Locate every blood parasite and identify its species.
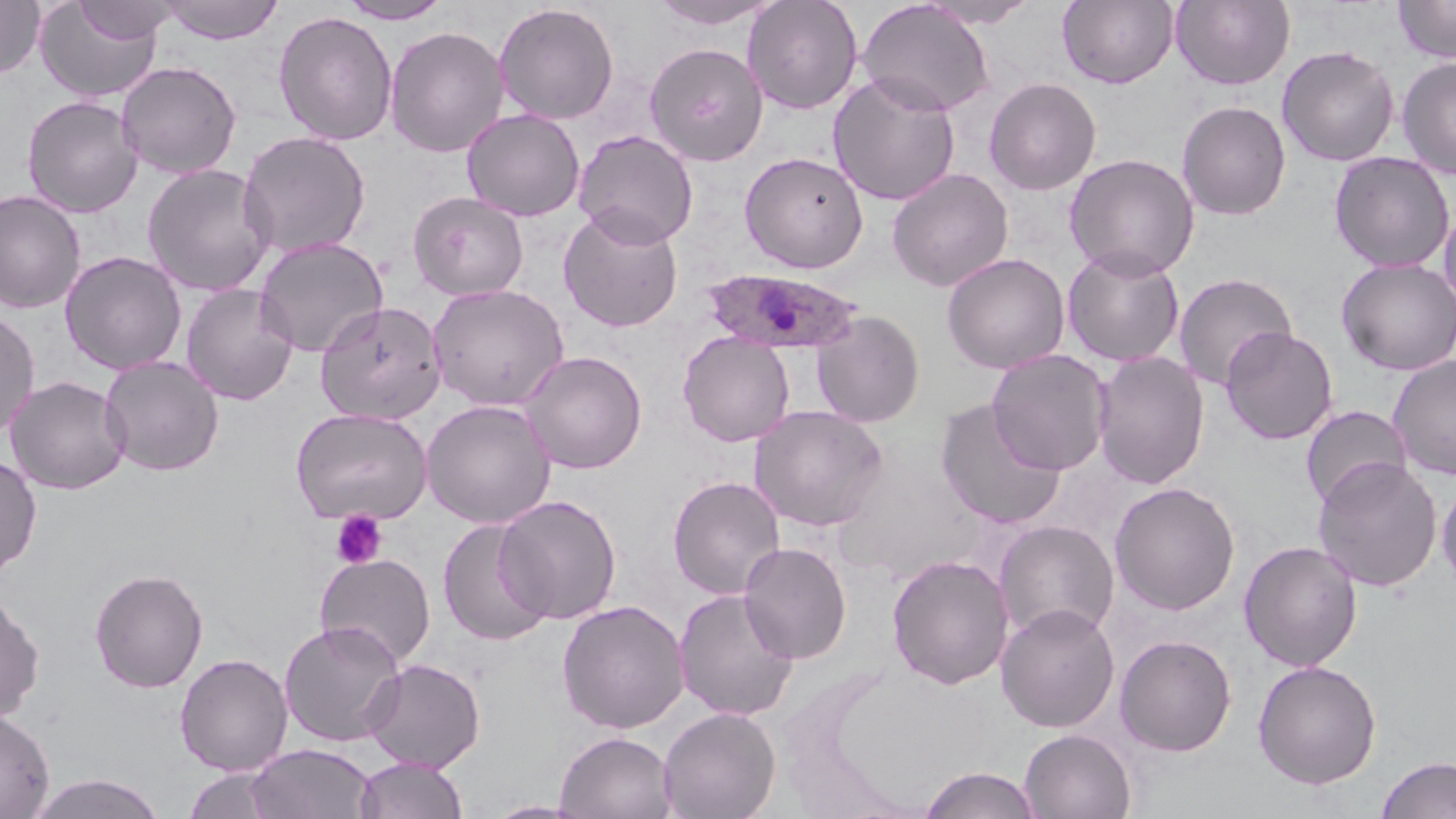

Approximate bounding boxes as [x1, y1, x2, y2] in pixels.
Plasmodium ovale-infected red blood cells: [703, 268, 865, 355].
No Plasmodium falciparum, Plasmodium malariae, Plasmodium vivax, Babesia divergens, or Trypanosoma brucei observed.

slide-level diagnosis = Plasmodium ovale
stain = May-Grünwald-Giemsa
preparation = thin blood smear
modality = light microscopy
magnification = 1000x
field of view = single
platelet locations = approximate bounding boxes as [x1, y1, x2, y2] in pixels: [331, 509, 388, 569]
image size = 1456×819 pixels
uninfected red blood cell locations = approximate bounding boxes as [x1, y1, x2, y2] in pixels: [0, 0, 45, 80], [72, 0, 179, 43], [160, 0, 284, 44], [649, 0, 781, 29], [742, 0, 863, 115], [918, 0, 1041, 28], [1057, 0, 1178, 88], [1171, 0, 1295, 90], [1393, 0, 1456, 63], [34, 1, 164, 103], [337, 1, 452, 24], [857, 1, 996, 116], [493, 2, 620, 125], [273, 11, 398, 146], [384, 25, 509, 158], [644, 42, 768, 166], [1277, 44, 1400, 167], [1397, 57, 1456, 179], [116, 61, 242, 179], [827, 73, 961, 206], [984, 77, 1101, 195], [22, 95, 143, 218], [1176, 100, 1291, 220], [462, 109, 585, 221], [573, 130, 699, 247], [237, 131, 372, 260], [739, 151, 869, 273], [1329, 151, 1455, 273], [1064, 153, 1200, 280], [142, 163, 276, 297], [887, 168, 1014, 292], [0, 189, 86, 314], [407, 191, 529, 300], [1439, 202, 1456, 316], [557, 206, 684, 332], [254, 236, 388, 358], [1062, 246, 1185, 367], [60, 251, 187, 375], [942, 252, 1070, 374], [1336, 258, 1456, 376], [1173, 273, 1298, 390], [428, 283, 569, 411], [181, 284, 298, 405], [315, 301, 447, 426], [0, 308, 40, 439], [810, 310, 926, 427], [1220, 327, 1338, 445], [677, 332, 795, 447], [986, 349, 1113, 475], [520, 350, 647, 474], [1092, 350, 1211, 490], [100, 355, 224, 476], [1387, 355, 1456, 480], [4, 375, 132, 495], [935, 397, 1067, 529], [421, 400, 556, 528], [749, 405, 889, 531], [1300, 405, 1412, 511], [291, 407, 432, 524], [0, 452, 42, 579], [1312, 457, 1443, 592], [667, 475, 786, 599], [1436, 476, 1456, 593], [1109, 482, 1240, 615], [495, 495, 623, 624], [437, 519, 554, 647], [993, 520, 1120, 644], [1239, 540, 1362, 672], [737, 541, 852, 664], [314, 553, 436, 668], [886, 554, 1014, 690], [89, 568, 209, 693], [674, 588, 800, 721], [0, 589, 45, 725], [557, 600, 689, 734], [995, 603, 1120, 731], [994, 617, 1234, 744], [278, 620, 405, 747], [1114, 634, 1237, 757], [175, 653, 293, 775], [361, 658, 485, 773], [1252, 659, 1382, 789], [657, 706, 781, 819], [0, 709, 55, 818], [1019, 728, 1137, 819], [555, 731, 677, 819], [246, 743, 377, 819], [354, 756, 469, 819], [1376, 756, 1456, 819], [918, 766, 1044, 818], [182, 768, 285, 818], [28, 773, 167, 818], [484, 800, 590, 818]